Assess this cell for malaria.
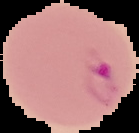
It is parasitized.

From a thin blood film. The area outside the segmented cell region is set to black. Image is 139×133 pixels.